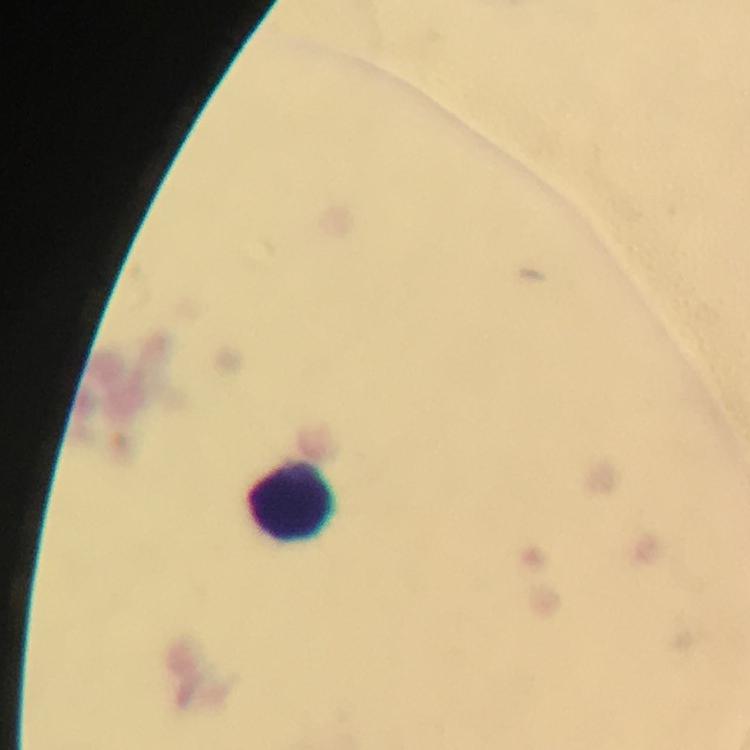

Approximate centers as (x, y) in pixels. Leukocyte locations: (295, 501). Giemsa-stained preparation. Photographed with a smartphone mounted on the microscope. Image is 750×750 pixels. 100x magnification. Thick smear. From a malaria diagnostic workup. A crop from one field of view. Immersion oil was used. Malaria parasites: none detected.